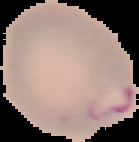

From a thin blood film. Segmented cell region on a black background. Image is 139×142 pixels. Malaria status: parasitized.